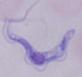

{
  "identification": "trypanosome",
  "magnification": "1000x",
  "modality": "photomicrograph"
}